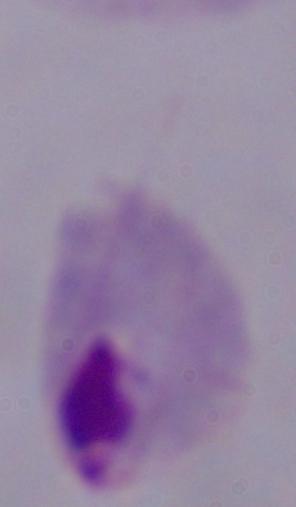

{
  "identification": "trichomonad",
  "magnification": "1000x",
  "modality": "micrograph"
}